Evaluate for parasitized red blood cells.
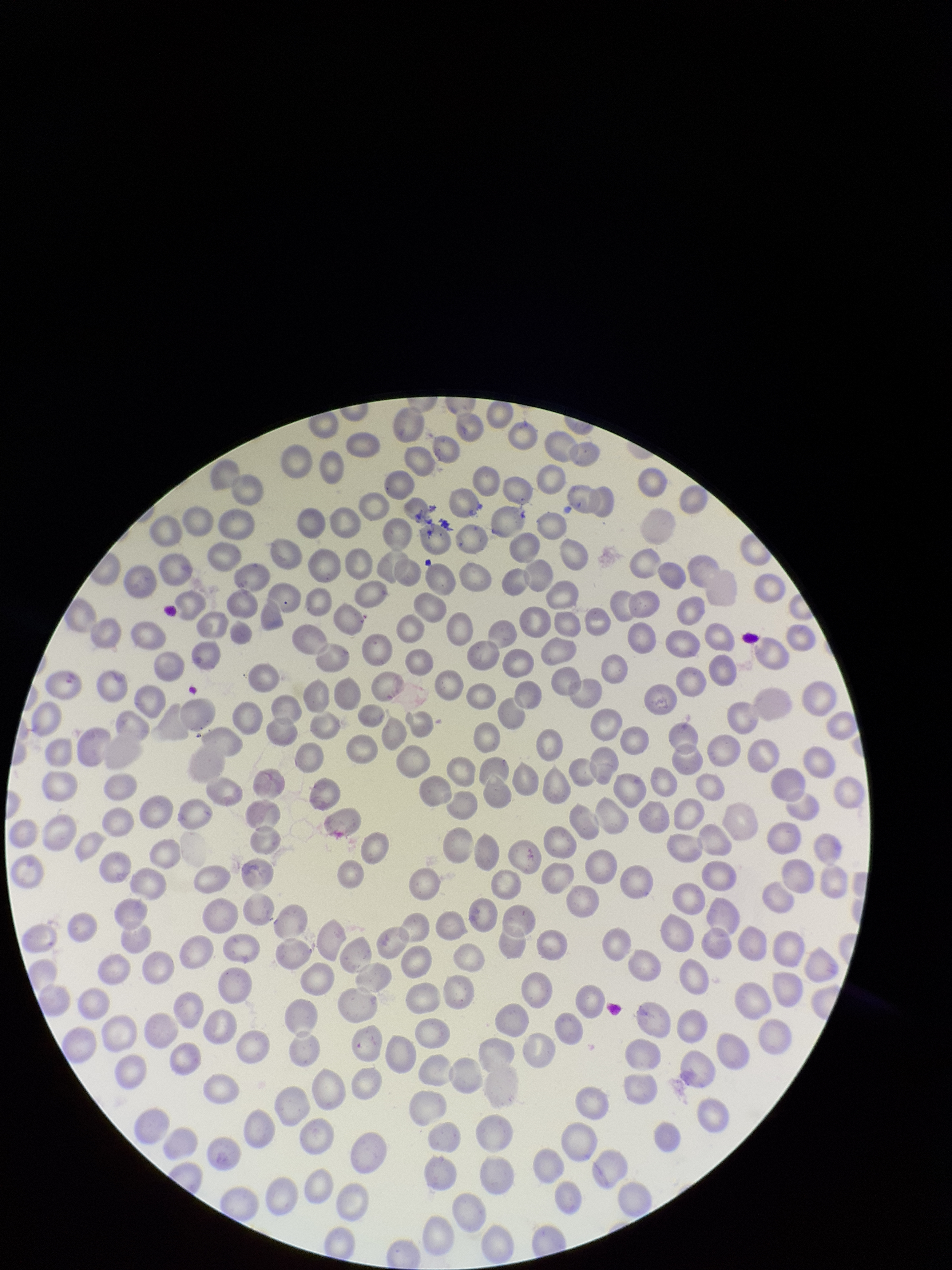

None identified.

Giemsa stain. Preparation: thin smear. Parasitized red blood cell count: 0. Smartphone photograph taken through the eyepiece of a microscope. Patient malaria status: infected. Species reported for this patient: Plasmodium falciparum. Red blood cell count: 295. Single field of view. Image is 952×1270 pixels.